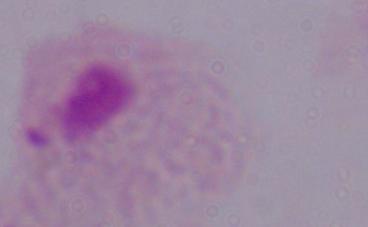

magnification = 1000x
identification = trichomonad
modality = micrograph